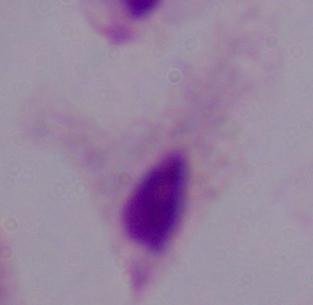

{
  "modality": "photomicrograph",
  "identification": "trichomonad",
  "magnification": "1000x"
}